Assess the background quality.
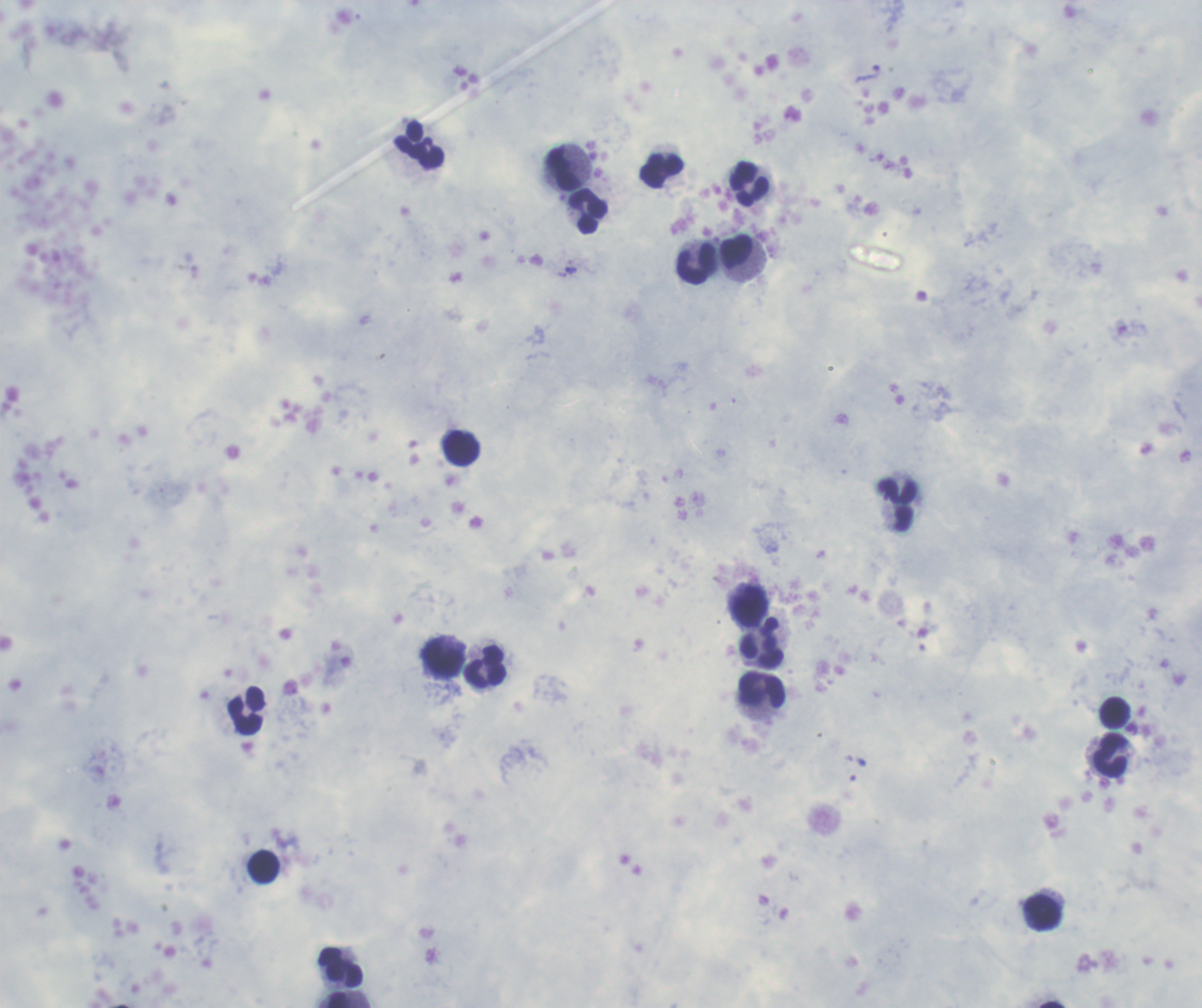

It is good.

Approximate centers as [x, y] in pixels. Leukocyte locations: [420, 144], [562, 167], [662, 170], [749, 183], [589, 211], [737, 251], [696, 264], [461, 447], [897, 504], [749, 607], [762, 642], [442, 658], [486, 666], [761, 690], [246, 711], [1114, 712], [1109, 754], [264, 867], [1044, 913], [341, 968], [337, 1000]. Trophozoite locations: [869, 73], [571, 270]. Coloration quality: good. Previously used in an actual diagnosis. Result: Plasmodium parasites identified. Image is 1202×1008 pixels. Romanowsky-stained preparation. Thick smear of blood. Captured at 100x magnification. One field from this slide.